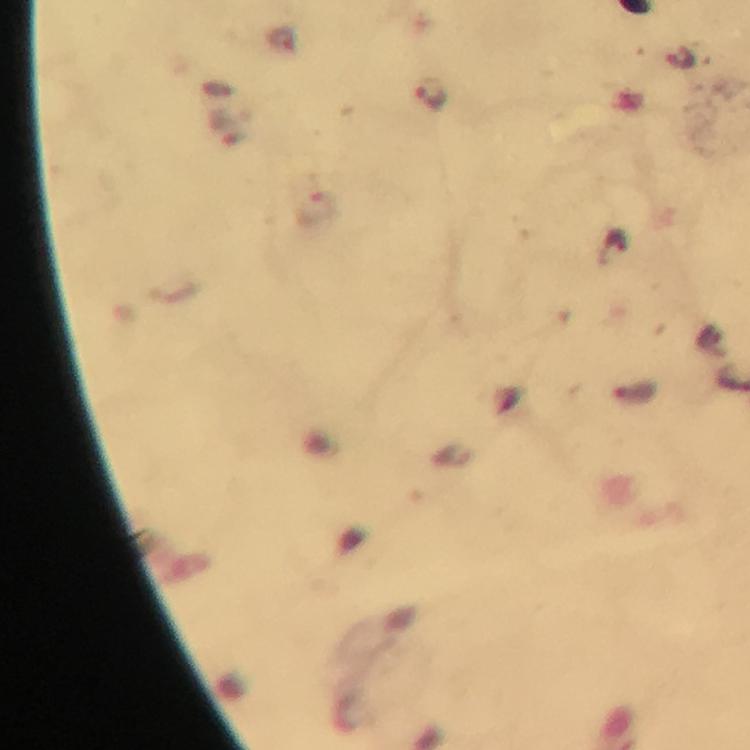

Approximate centers as {x, y} in pixels. Malaria parasite locations: {430, 94}. Image is 750×750 pixels. Immersion oil applied. Giemsa stain. Thick blood film. A crop from one field of view. From a diagnostic examination for malaria. Smartphone photograph taken through a microscope. 100x magnification.